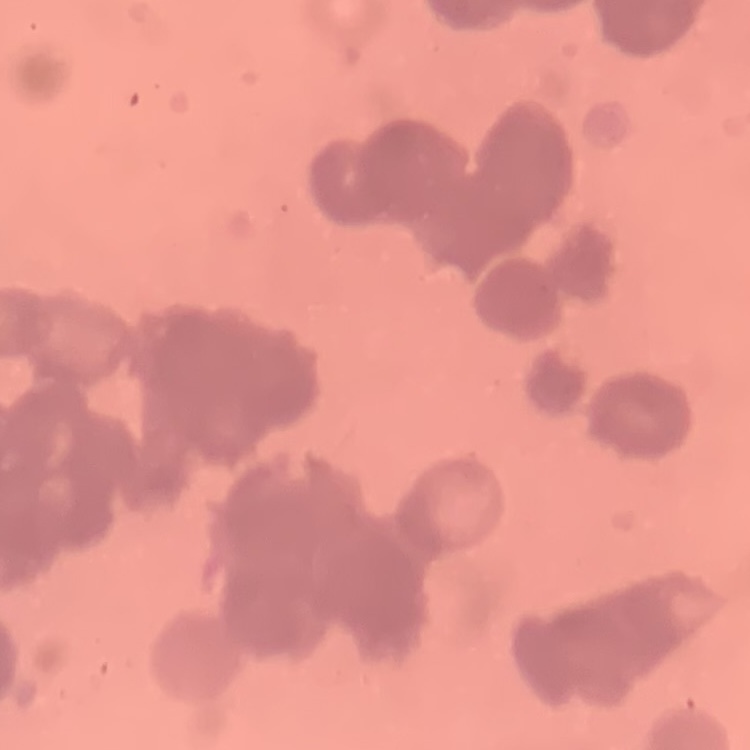

Summary:
  - Red blood cell morphology: rouleaux formation
  - Image type: one tile cut from a larger photomicrograph
  - Preparation: thin blood film
  - Stain: Field's or Giemsa